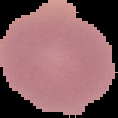

{
  "image_type": "segmented cell region with the area outside set to black",
  "malaria_status": "uninfected",
  "image_size": "118×118 pixels",
  "preparation": "thin blood film"
}